Point out malaria parasites and leukocytes.
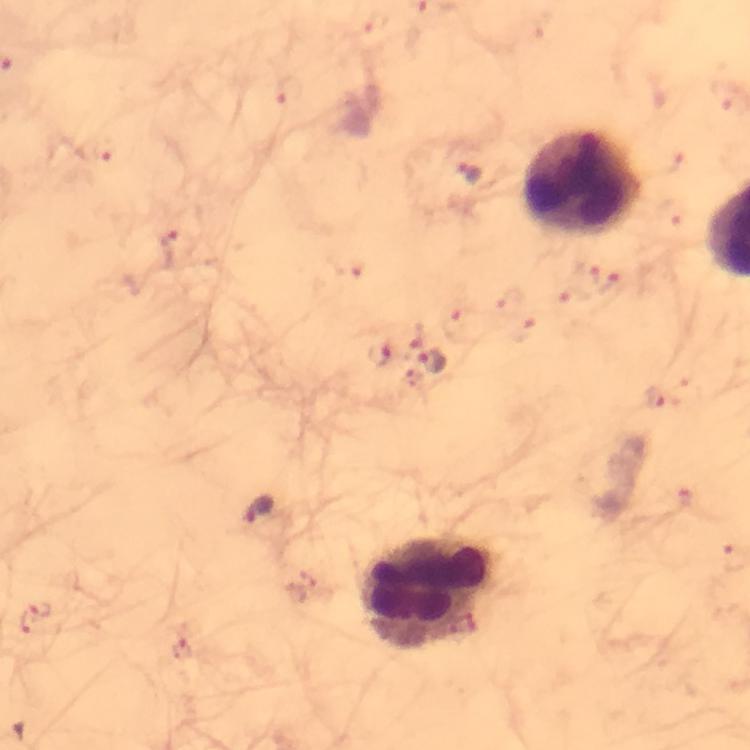

Approximate centers as [x, y] in pixels.
Malaria parasites: [171, 248], [381, 353], [431, 363], [259, 510], [37, 618], [184, 649].
Leukocytes: [584, 183], [428, 594].

preparation = thick blood smear
magnification = 100x
capture = smartphone camera through the microscope
cropped from = one field of view
context = from a diagnostic examination for malaria
stain = Giemsa
image size = 750×750 pixels
immersion oil = used